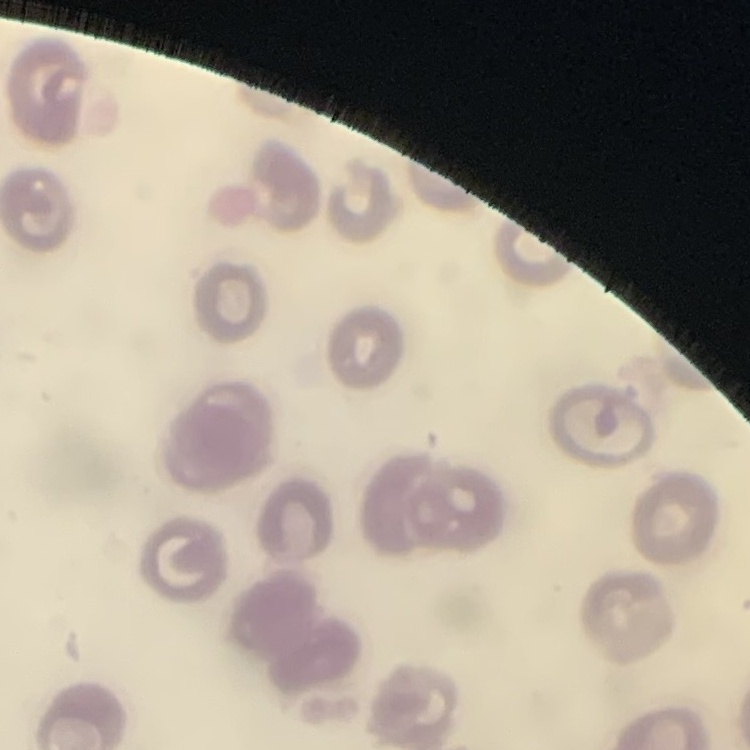 The red blood cells show no rouleaux formation. Thin peripheral smear. Stained with either Field's or Giemsa. Square crop of a larger photomicrograph.